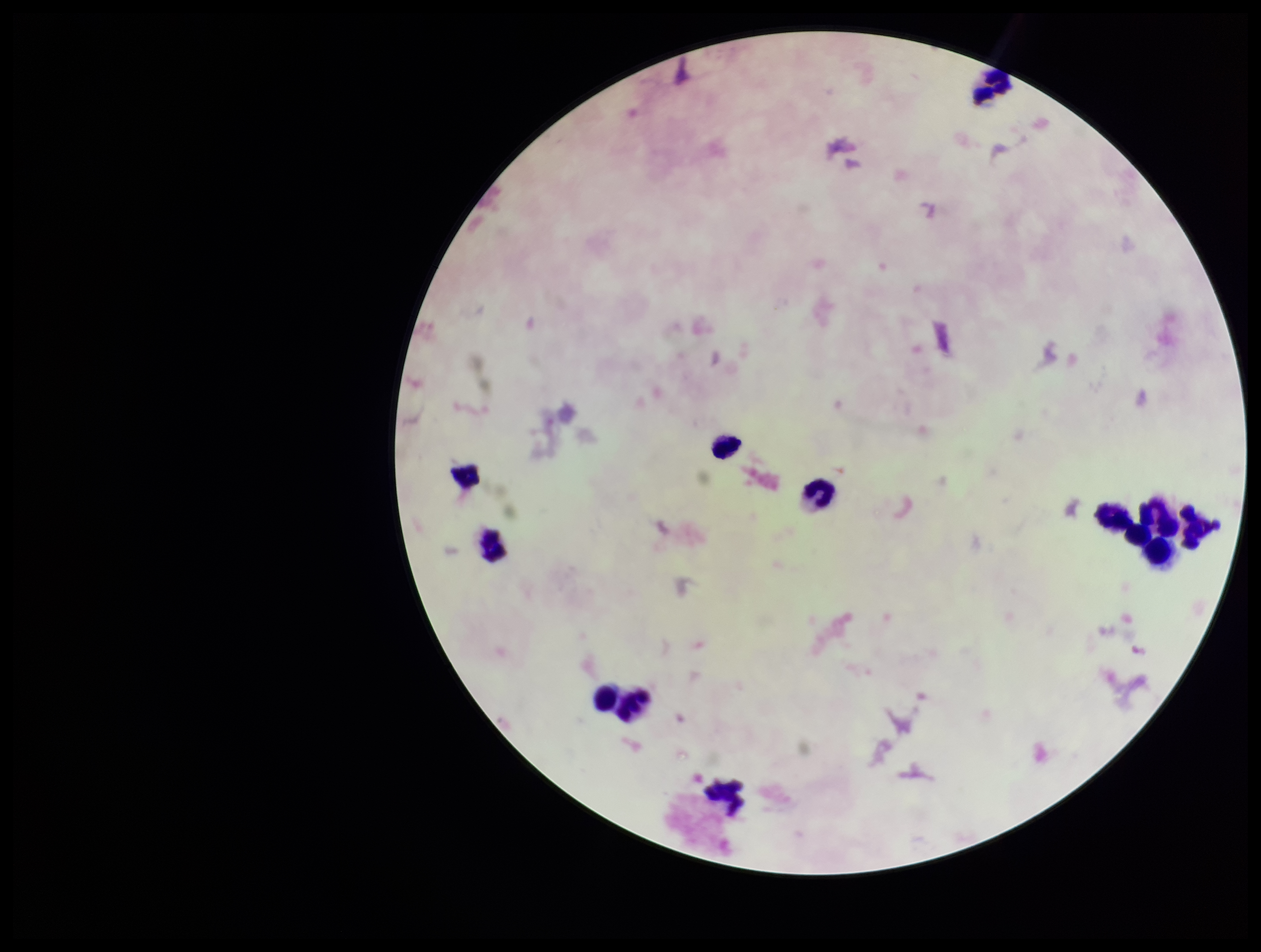
leukocyte_count: 12
patient_malaria_status: positive
plasmodium_parasites: none detected
capture: smartphone photograph through the microscope eyepiece
preparation: thick blood smear
field_of_view: single
image_size: 1261×952 pixels
parasite_count: 0
stain: Giemsa
species_reported_for_this_patient: Plasmodium falciparum